Outline each uninfected red blood cell.
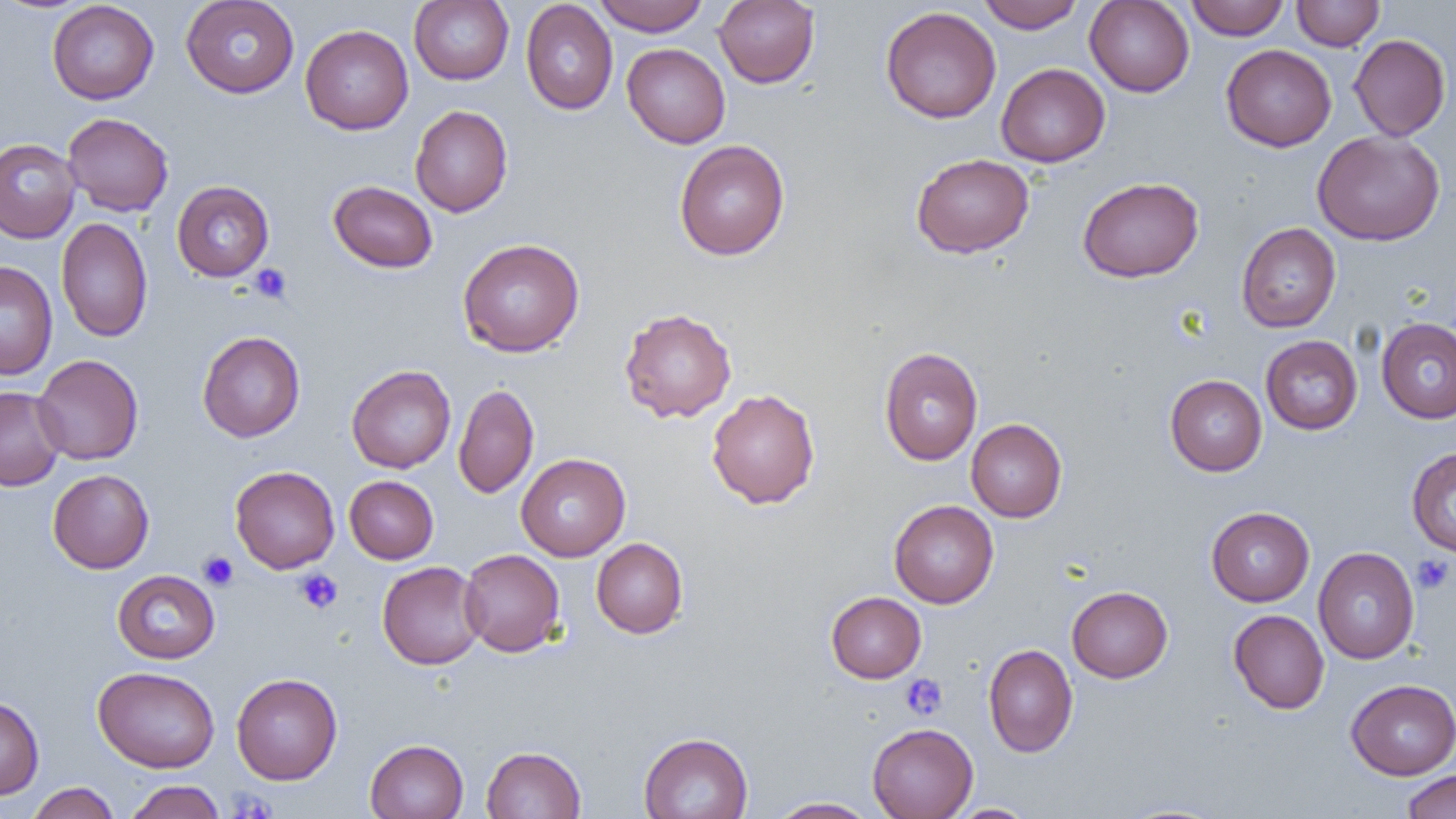

Approximate bounding boxes as (x1, y1, x2, y2) in pixels.
Uninfected red blood cells: (180, 0, 299, 98), (409, 0, 514, 85), (593, 0, 710, 36), (713, 0, 820, 88), (974, 0, 1086, 32), (1185, 0, 1290, 40), (1292, 0, 1385, 51), (47, 1, 159, 104), (520, 1, 618, 115), (1084, 1, 1194, 97), (880, 6, 1001, 123), (300, 24, 413, 134), (1349, 34, 1450, 141), (622, 43, 730, 148), (1221, 44, 1336, 151), (996, 63, 1110, 167), (410, 104, 513, 217), (62, 112, 174, 217), (1312, 130, 1445, 246), (0, 138, 81, 243), (674, 139, 790, 261), (911, 153, 1035, 258), (1077, 176, 1204, 282), (171, 180, 274, 282), (328, 180, 438, 273), (56, 217, 153, 342), (1236, 222, 1341, 333), (457, 238, 585, 357), (0, 261, 58, 380), (619, 307, 737, 423), (1376, 317, 1456, 423), (197, 331, 305, 442), (1260, 335, 1363, 434), (879, 347, 983, 465), (32, 354, 144, 465), (346, 365, 456, 473), (1165, 374, 1267, 476), (453, 383, 539, 499), (0, 386, 66, 491), (706, 388, 820, 509), (966, 418, 1067, 522), (1406, 447, 1456, 556), (516, 453, 630, 561), (230, 465, 339, 573), (47, 469, 154, 573), (345, 475, 438, 564), (889, 500, 999, 608), (1206, 506, 1315, 606), (591, 538, 688, 638), (1313, 547, 1420, 664), (459, 549, 565, 657), (377, 561, 486, 669), (112, 570, 220, 664), (1067, 586, 1173, 683), (826, 591, 926, 683), (1228, 609, 1329, 714), (983, 644, 1078, 757), (93, 666, 220, 773), (231, 672, 342, 785), (1346, 679, 1456, 780), (0, 696, 44, 799), (867, 723, 978, 819), (639, 732, 753, 818), (365, 739, 468, 819), (481, 745, 586, 818), (1401, 770, 1456, 819), (124, 780, 226, 819), (26, 782, 120, 819), (768, 797, 880, 818), (948, 803, 1039, 818).

Summary:
  - Platelet locations: (249, 263, 293, 304), (198, 551, 239, 591), (1411, 554, 1454, 595), (294, 568, 343, 614), (900, 674, 948, 721), (227, 789, 279, 818)
  - Slide-level diagnosis: no evidence of blood parasites
  - Image size: 1456×819 pixels
  - Modality: light microscopy
  - Magnification: 1000x
  - Field of view: single
  - Preparation: thin blood smear